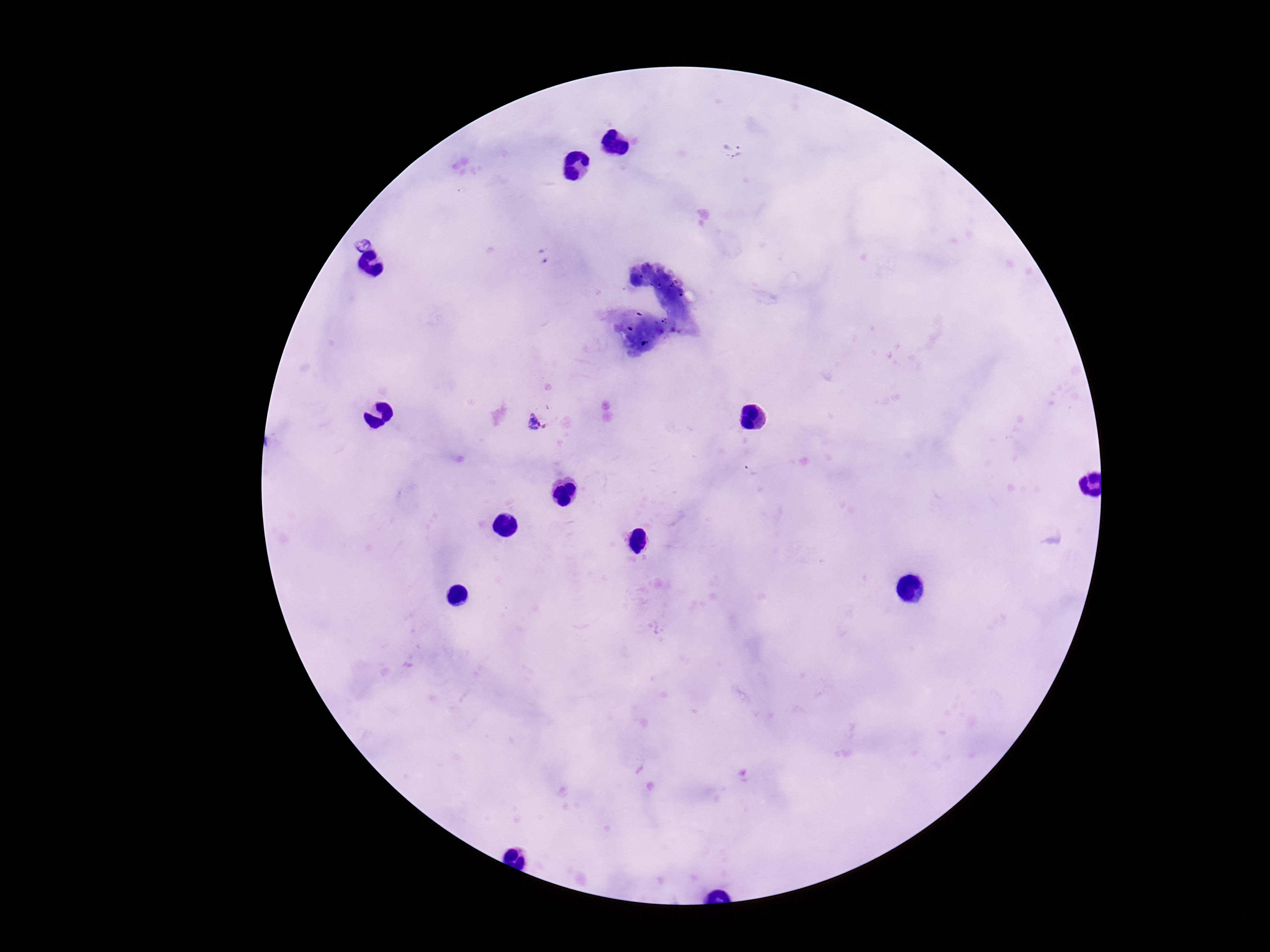 Approximate object centers, in pixels from the top-left corner. Plasmodium parasite locations: (x=733, y=141), (x=738, y=158), (x=544, y=256), (x=536, y=423). Smartphone photograph taken through the microscope eyepiece. Image is 1270×952 pixels. 100x magnification. Giemsa-stained preparation. Single field of view. Patient malaria status: infected. Thick blood smear.